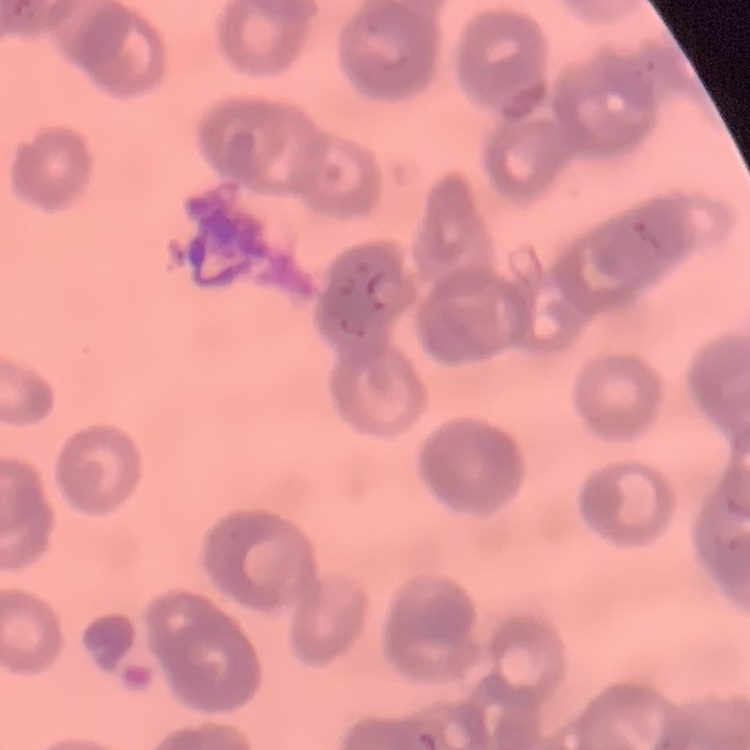 The red blood cells show rouleaux formation. Stained with either Field's or Giemsa. Thin blood film. Square crop of a larger photomicrograph.